Classify this cell by malaria status.
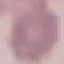
It is uninfected.

image type = automatically extracted cell patch, resized to 64 × 64 pixels
preparation = thin blood film
capture = smartphone through the microscope eyepiece
stain = Giemsa